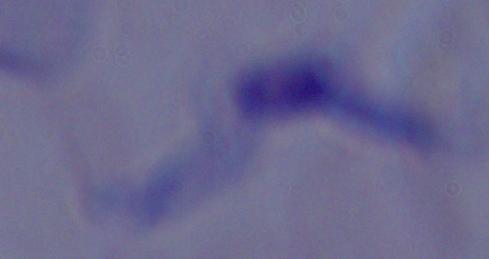

Summary:
  - Modality: photomicrograph
  - Identification: trypanosome
  - Magnification: 1000x